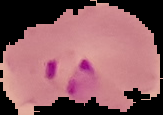
Summary:
  - Preparation: thin blood smear
  - Image size: 163×115 pixels
  - Image type: cell region segmented out of the field of view; surrounding area masked to black
  - Malaria status: parasitized